Describe the morphology of the erythrocytes.
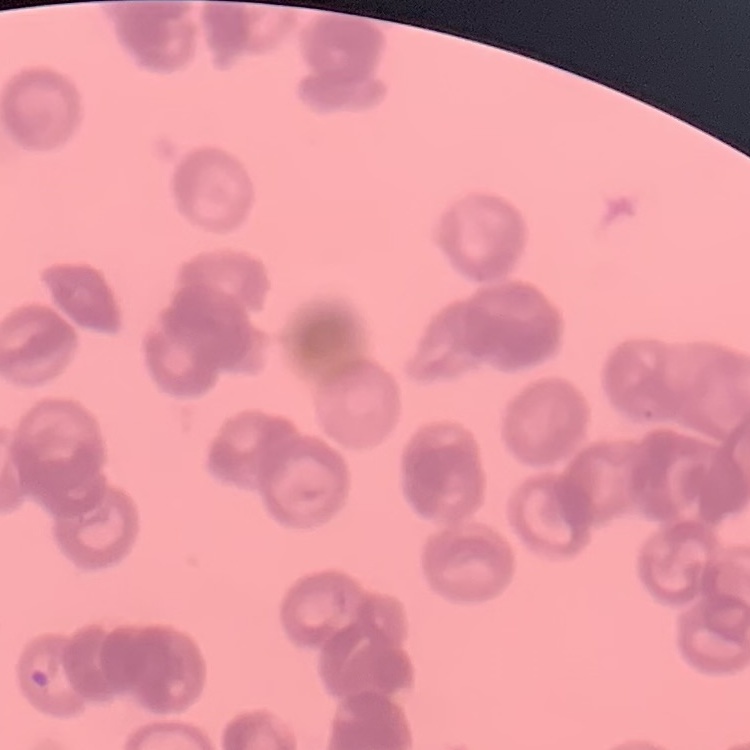
Rouleaux formation.

preparation = thin peripheral smear
image type = square crop of a larger photomicrograph
stain = Field's or Giemsa